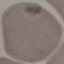
malaria status = uninfected
preparation = thin smear
stain = Giemsa
capture = smartphone camera at the microscope eyepiece
image type = automatically extracted cell patch, resized to 64 × 64 pixels